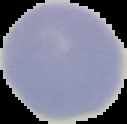

image_size: 127×124 pixels
preparation: thin blood smear
image_type: cell region segmented out of the field of view; surrounding area masked to black
result: no Plasmodium parasites seen